Assess for malaria.
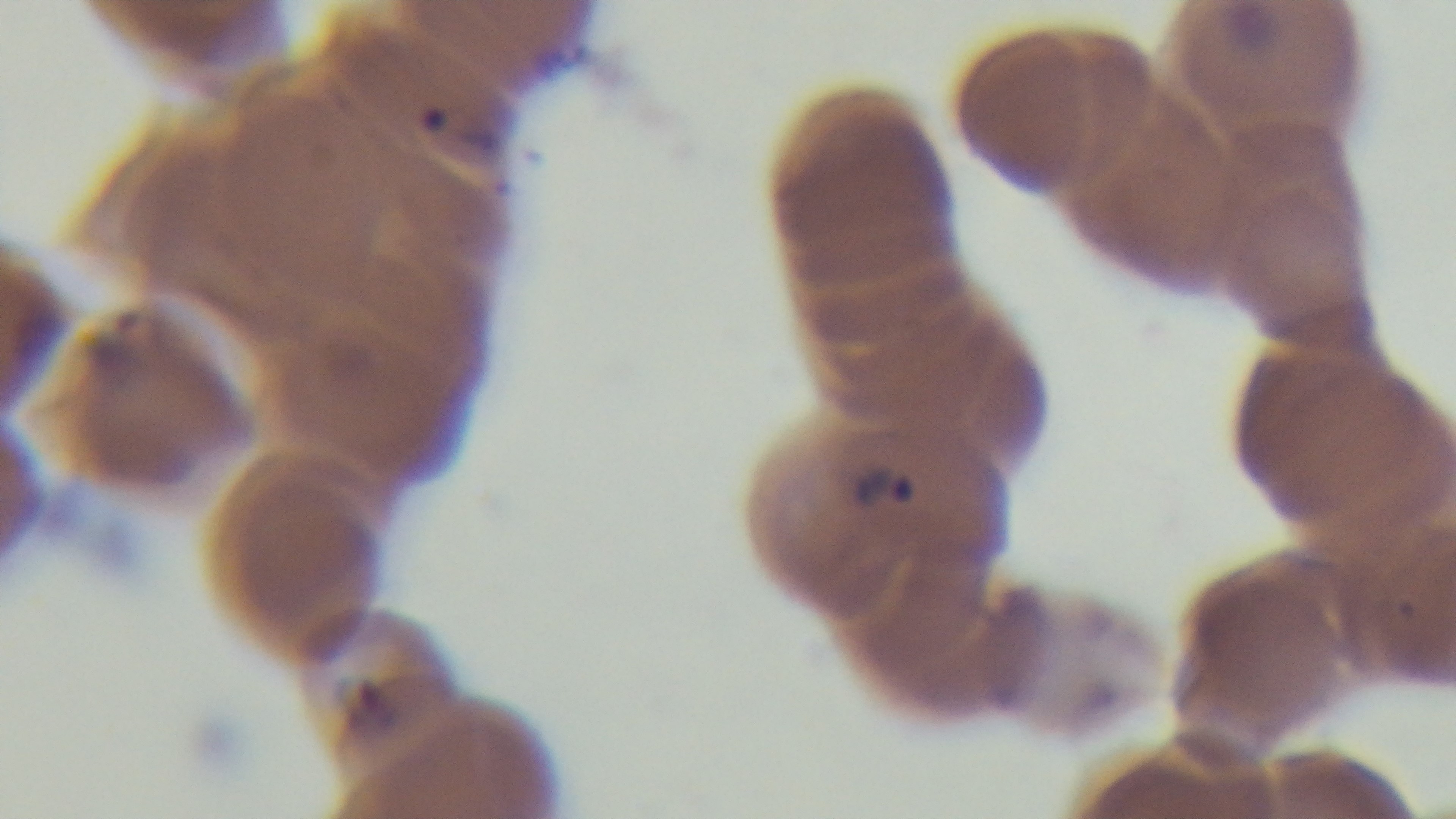

Infected.

Giemsa stain. One field from the slide. Captured with a mounted 4K digital camera. Preparation: thin. Photomicrograph. 100x oil-immersion objective.